Locate every malaria parasite by life-cycle stage, and every leukocyte.
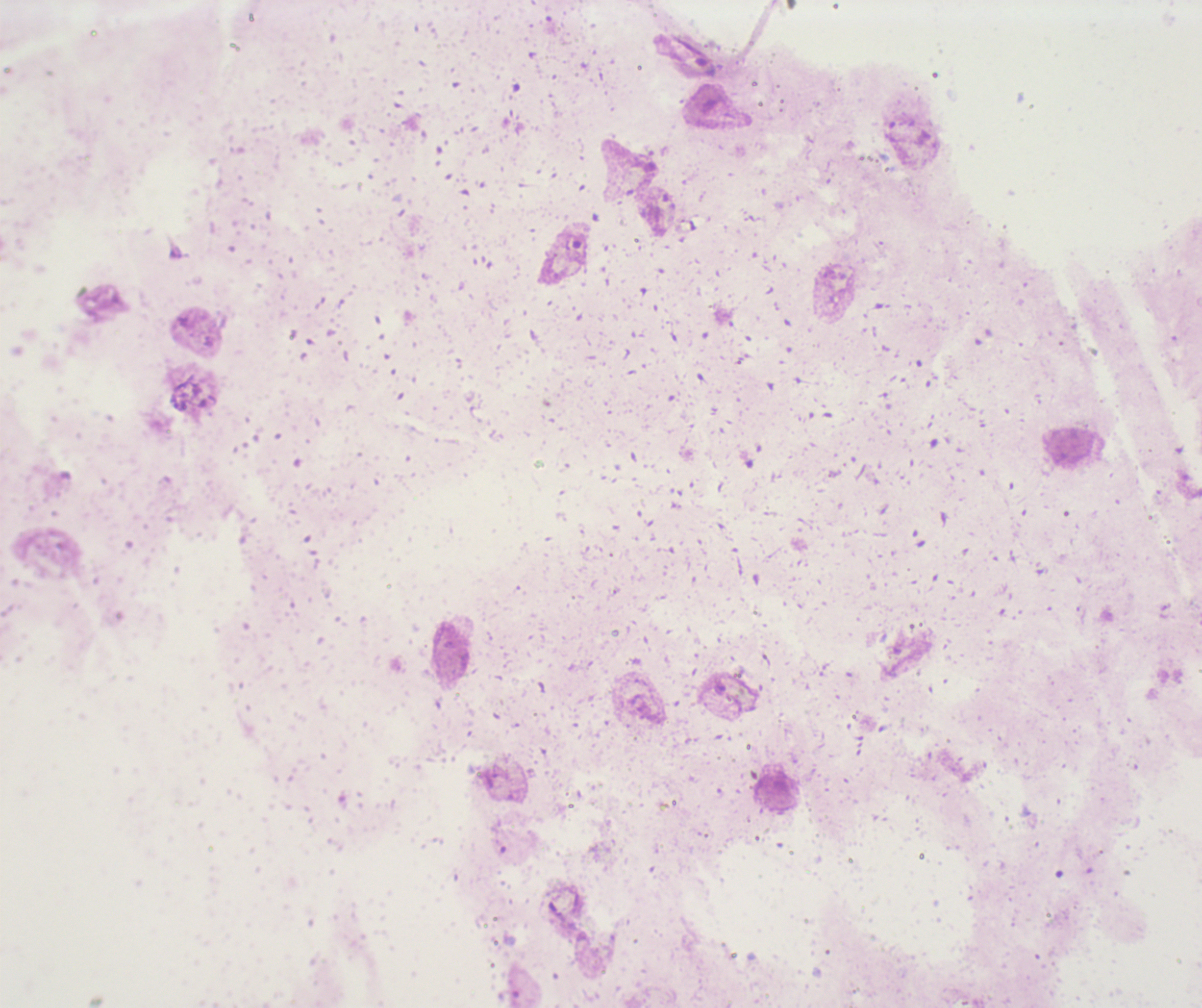

Approximate centers as (x, y) in pixels.
Trophozoites: (693, 59), (575, 248), (178, 401).
No schizont or gametocyte forms observed.
No leukocytes visible.

Romanowsky-stained preparation. Image is 1202×1008 pixels. Thick smear of blood. One field from this slide. Previously used in an actual diagnosis. Captured at 100x magnification. Coloration quality: bad. Background quality: unsatisfactory.